State which parasite is depicted.
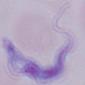
This is a trypanosome.

Photomicrograph. 1000x magnification.